State which cell type is depicted.
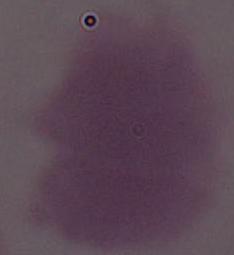
An erythrocyte.

magnification = 1000x
modality = photomicrograph